Point out each leukocyte.
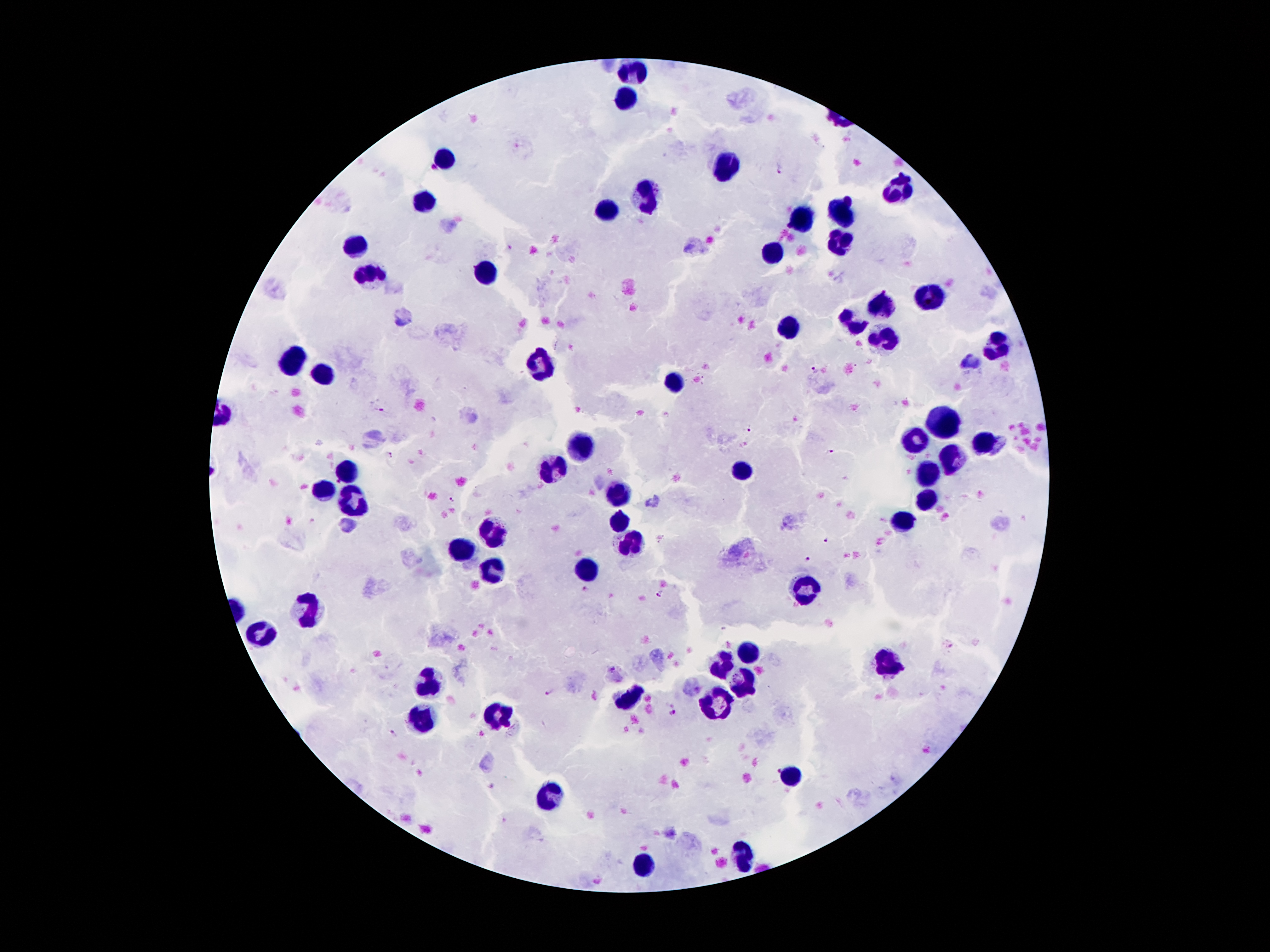

Approximate object centers, in pixels from the top-left corner.
Leukocytes: (x=634, y=71), (x=625, y=100), (x=442, y=159), (x=726, y=170), (x=897, y=187), (x=647, y=197), (x=424, y=202), (x=606, y=211), (x=844, y=211), (x=802, y=219), (x=839, y=243), (x=354, y=247), (x=777, y=254), (x=484, y=272), (x=370, y=274), (x=930, y=294), (x=884, y=306), (x=849, y=320), (x=790, y=329), (x=884, y=337), (x=994, y=345), (x=291, y=359), (x=538, y=364), (x=322, y=369), (x=673, y=381), (x=943, y=417), (x=916, y=438), (x=985, y=441), (x=582, y=444), (x=952, y=459), (x=742, y=467), (x=345, y=468), (x=551, y=471), (x=929, y=476), (x=318, y=490), (x=616, y=494), (x=925, y=499), (x=353, y=502), (x=618, y=518), (x=899, y=523), (x=492, y=530), (x=629, y=541), (x=460, y=550), (x=586, y=567), (x=492, y=574), (x=807, y=585), (x=307, y=611), (x=261, y=635), (x=746, y=649), (x=889, y=656), (x=721, y=663), (x=744, y=683), (x=427, y=684), (x=631, y=697), (x=715, y=705), (x=500, y=711), (x=423, y=719), (x=790, y=775), (x=549, y=796), (x=744, y=852), (x=641, y=864).

malaria parasite locations = (x=781, y=170), (x=815, y=368), (x=381, y=408), (x=746, y=427), (x=829, y=452), (x=385, y=455), (x=451, y=501), (x=826, y=542), (x=806, y=559), (x=586, y=590), (x=660, y=593), (x=549, y=694), (x=675, y=714), (x=393, y=734), (x=777, y=770)
magnification = 100x
preparation = thick blood film
image size = 1270×952 pixels
capture = smartphone through the microscope eyepiece
stain = Giemsa
patient malaria status = positive for Plasmodium falciparum
field of view = single